Identify the blood parasite species.
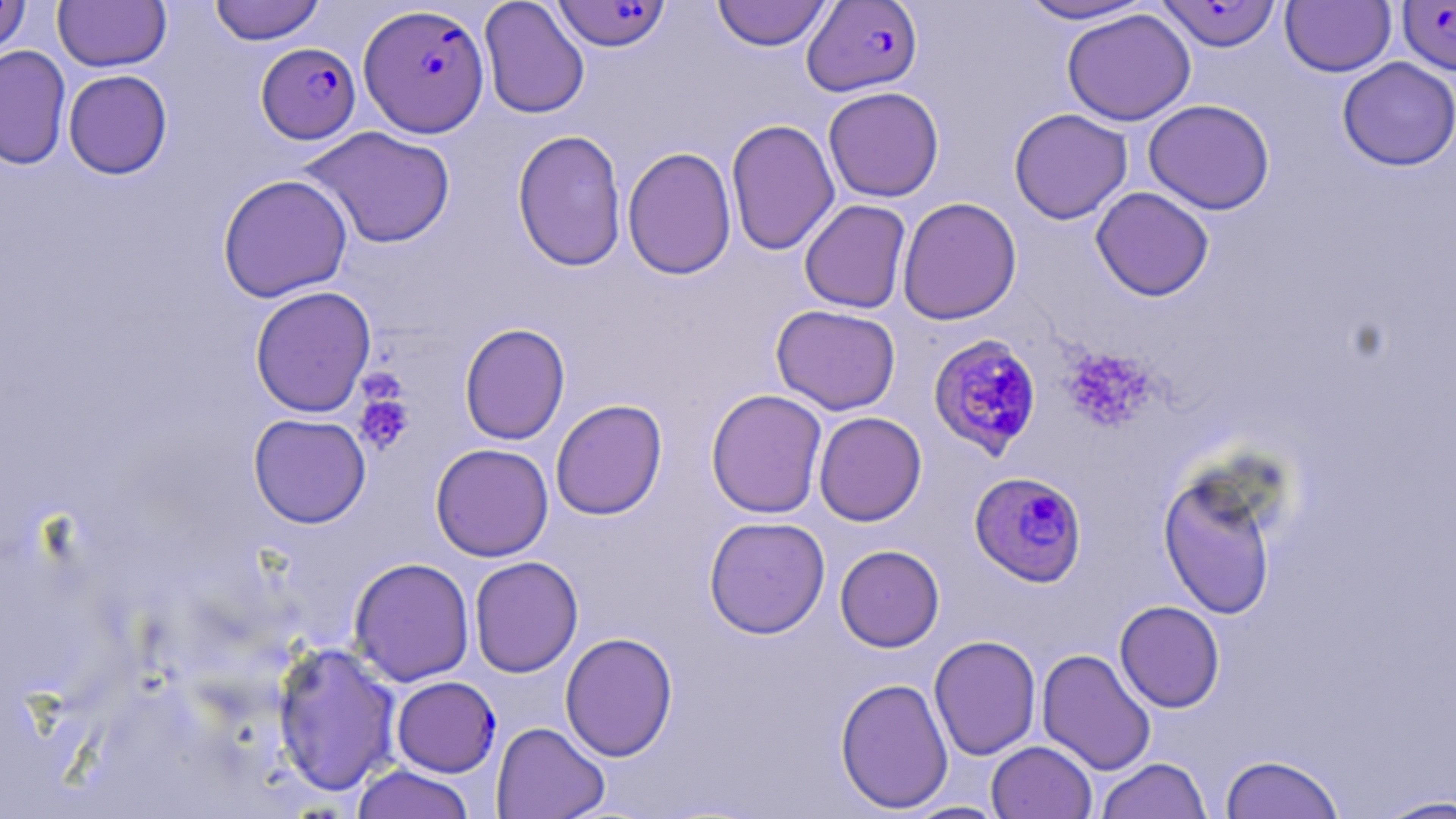
Plasmodium falciparum.

uninfected red blood cell locations = approximate bounding boxes as (x1, y1, x2, y2) in pixels: (0, 0, 31, 57), (53, 0, 172, 72), (208, 0, 326, 45), (478, 0, 590, 119), (711, 0, 833, 51), (1016, 0, 1157, 24), (1281, 0, 1396, 77), (1062, 8, 1195, 126), (0, 45, 72, 170), (1337, 57, 1456, 171), (63, 69, 173, 179), (823, 86, 944, 203), (1143, 99, 1275, 215), (1008, 108, 1133, 224), (725, 119, 840, 256), (299, 125, 456, 249), (512, 129, 627, 272), (622, 146, 737, 280), (217, 173, 353, 302), (1091, 186, 1215, 301), (897, 197, 1022, 325), (798, 199, 912, 314), (249, 285, 377, 417), (771, 304, 901, 415), (459, 323, 570, 445), (705, 388, 828, 519), (550, 399, 668, 521), (813, 411, 927, 526), (248, 413, 371, 528), (430, 442, 554, 561), (1157, 465, 1282, 620), (704, 516, 830, 639), (835, 545, 945, 652), (349, 556, 475, 686), (469, 556, 584, 678), (1114, 600, 1225, 713), (560, 631, 678, 761), (929, 635, 1041, 760), (271, 642, 401, 797), (1036, 648, 1157, 775), (391, 675, 501, 777), (835, 676, 954, 813), (491, 722, 610, 819), (986, 741, 1097, 819), (1219, 753, 1345, 819), (1095, 757, 1212, 819), (349, 764, 477, 819), (1373, 794, 1456, 818), (901, 801, 1009, 818)
preparation = thin blood smear
stain = May-Grünwald-Giemsa
magnification = 1000x
platelet locations = approximate bounding boxes as (x1, y1, x2, y2) in pixels: (1061, 347, 1157, 431), (354, 393, 414, 455)
Plasmodium falciparum-infected red blood cell locations = approximate bounding boxes as (x1, y1, x2, y2) in pixels: (802, 0, 923, 97), (552, 1, 672, 51), (1397, 1, 1456, 75), (1155, 2, 1282, 51), (356, 4, 488, 140), (259, 45, 364, 147), (927, 334, 1043, 460), (969, 470, 1088, 587)
image size = 1456×819 pixels
field of view = single
modality = optical microscopy